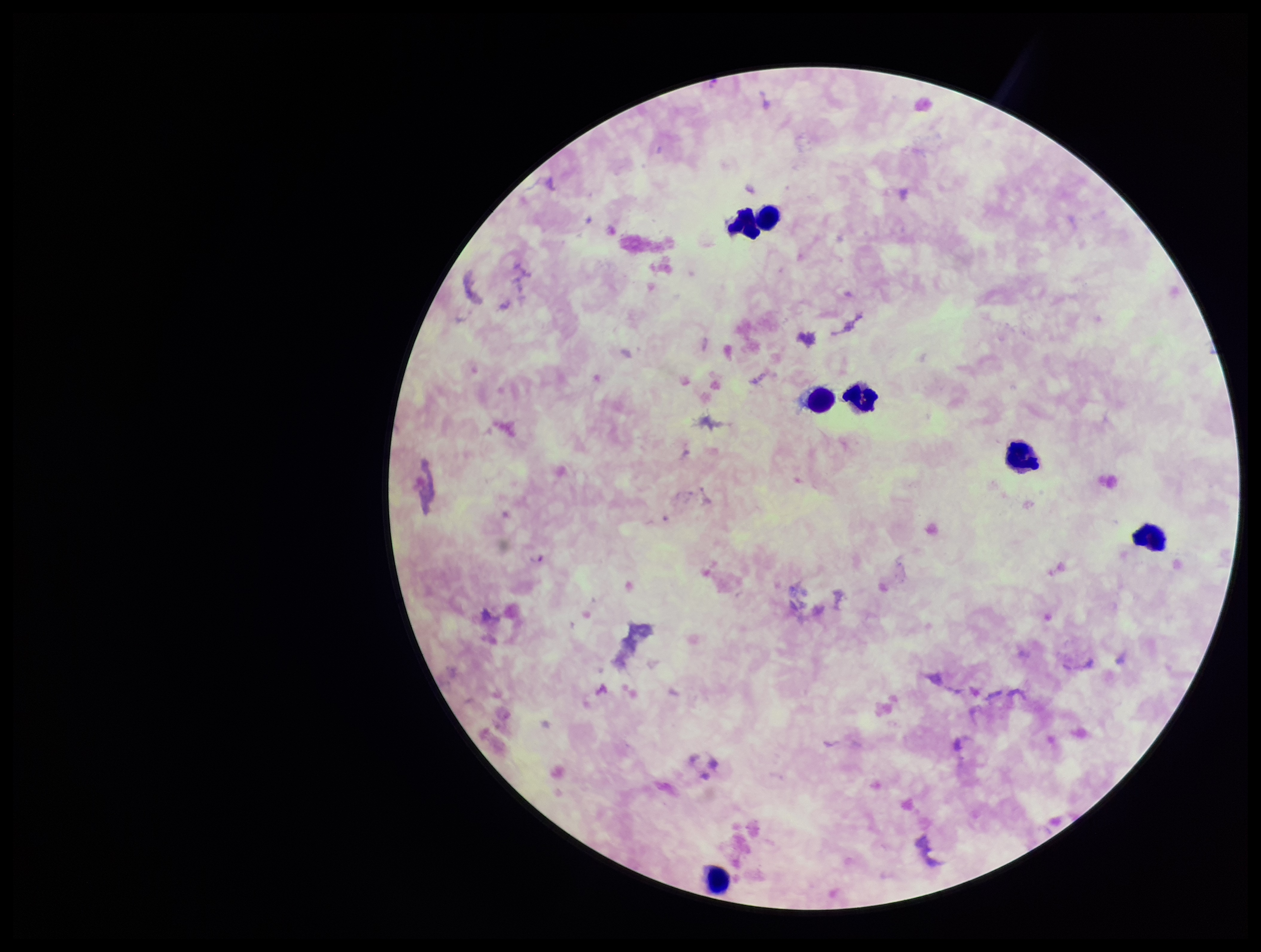

Parasite count: 0. Single field of view. Leukocyte count: 7. Image is 1261×952 pixels. Species reported for this patient: Plasmodium falciparum. Giemsa stain. Plasmodium parasites: none identified. Photographed through the microscope eyepiece with a smartphone camera. Patient malaria status: infected. Preparation: thick smear.